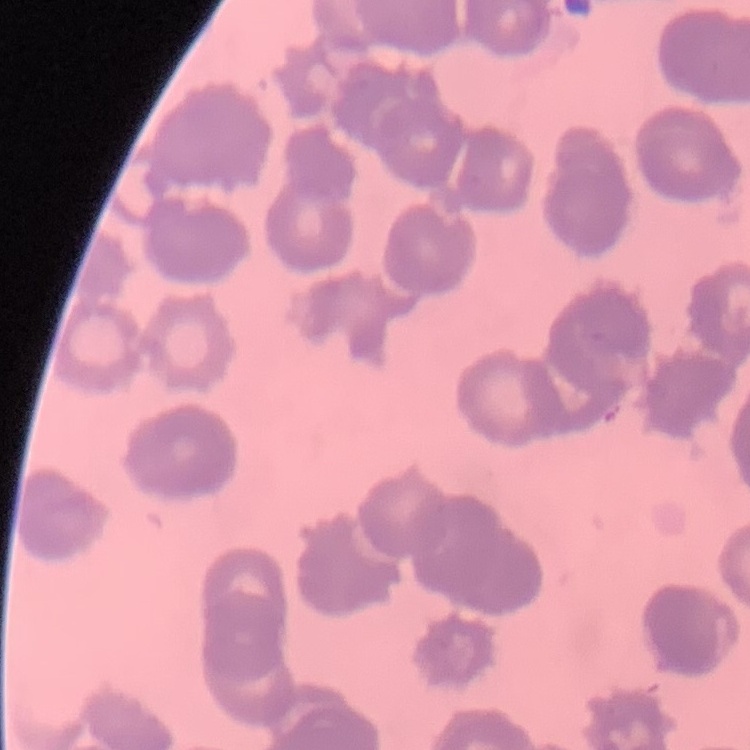

red blood cell morphology = rouleaux formation
image type = square crop of a larger photomicrograph
preparation = thin blood film
stain = Field's or Giemsa